Give a bounding box for every artifact (stain precipitate or debris).
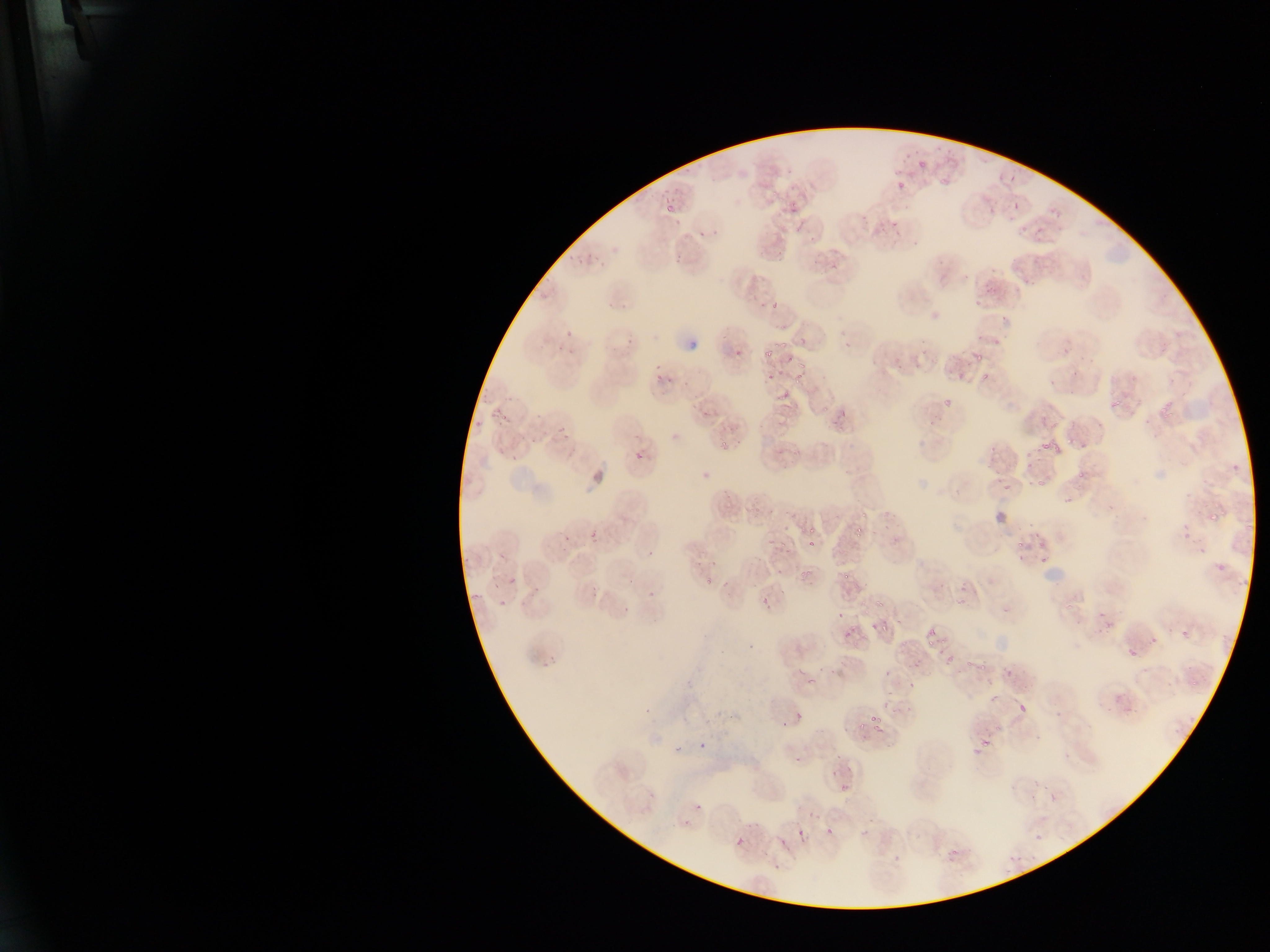

Approximate bounding boxes as left top right bottom in pixels.
Artifacts (stain precipitate or debris): 676 325 697 352.

Plasmodium parasite locations (subset; some below the resolvable size): 915 158 930 168; 938 175 952 189; 1009 175 1017 183; 898 179 913 191; 772 188 780 196; 790 200 810 213; 1013 202 1019 212; 666 204 677 215; 672 256 684 264; 975 297 984 305; 773 302 778 310; 975 334 986 343; 994 339 1005 347; 764 350 773 360; 973 354 986 362; 785 356 794 366; 797 361 807 372; 955 371 964 380; 982 372 990 381; 765 374 776 382; 794 375 801 384; 775 390 791 401; 943 395 952 408; 1109 396 1128 408; 1157 401 1177 414; 821 406 832 411; 556 426 566 435; 1064 436 1074 444; 719 439 728 451; 1041 440 1052 451; 986 448 1000 468; 1024 452 1034 470; 634 455 646 461; 1077 467 1086 477; 1034 478 1048 489; 1002 479 1011 493; 1208 509 1218 520; 862 510 865 518; 857 527 865 539; 589 530 596 539; 807 530 817 535; 1181 531 1196 539; 780 539 787 547; 1017 539 1026 550; 806 540 816 546; 1035 541 1048 549; 1198 546 1208 554; 498 553 506 559; 1041 555 1052 564; 1214 561 1227 572; 799 569 812 579; 844 570 854 582; 508 577 514 585; 703 578 713 586; 493 581 498 590; 761 591 771 604; 498 600 509 608; 874 601 885 608; 1097 609 1106 621; 839 611 844 620; 870 621 880 631; 882 623 888 632; 926 624 937 637; 842 628 851 639; 1178 628 1188 639; 1149 637 1157 643; 928 638 938 646; 1127 644 1137 656; 945 654 954 664; 966 659 974 667; 980 664 989 671; 807 678 818 682; 1189 681 1197 687; 989 694 998 702; 1019 703 1026 714; 796 711 801 721; 869 716 884 724; 995 725 1004 732; 981 739 994 748; 971 747 980 754; 830 770 840 778; 836 786 846 793; 1048 791 1059 804; 825 828 834 835; 735 838 745 844 | approximate x y pixel centers of objects too small to bound: 896 171; 700 234; 782 344; 738 354; 779 372; 660 377; 514 458; 566 537; 771 541; 651 593; 911 686; 863 726; 678 749; 698 806; 800 832. Thin blood smear. Photographed through a microscope with a mobile-phone camera. Image is 1270×952 pixels. Collected in Ghana. Single field of view.